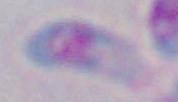

{
  "modality": "micrograph",
  "magnification": "1000x",
  "identification": "Toxoplasma gondii"
}